Identify the blood parasite species.
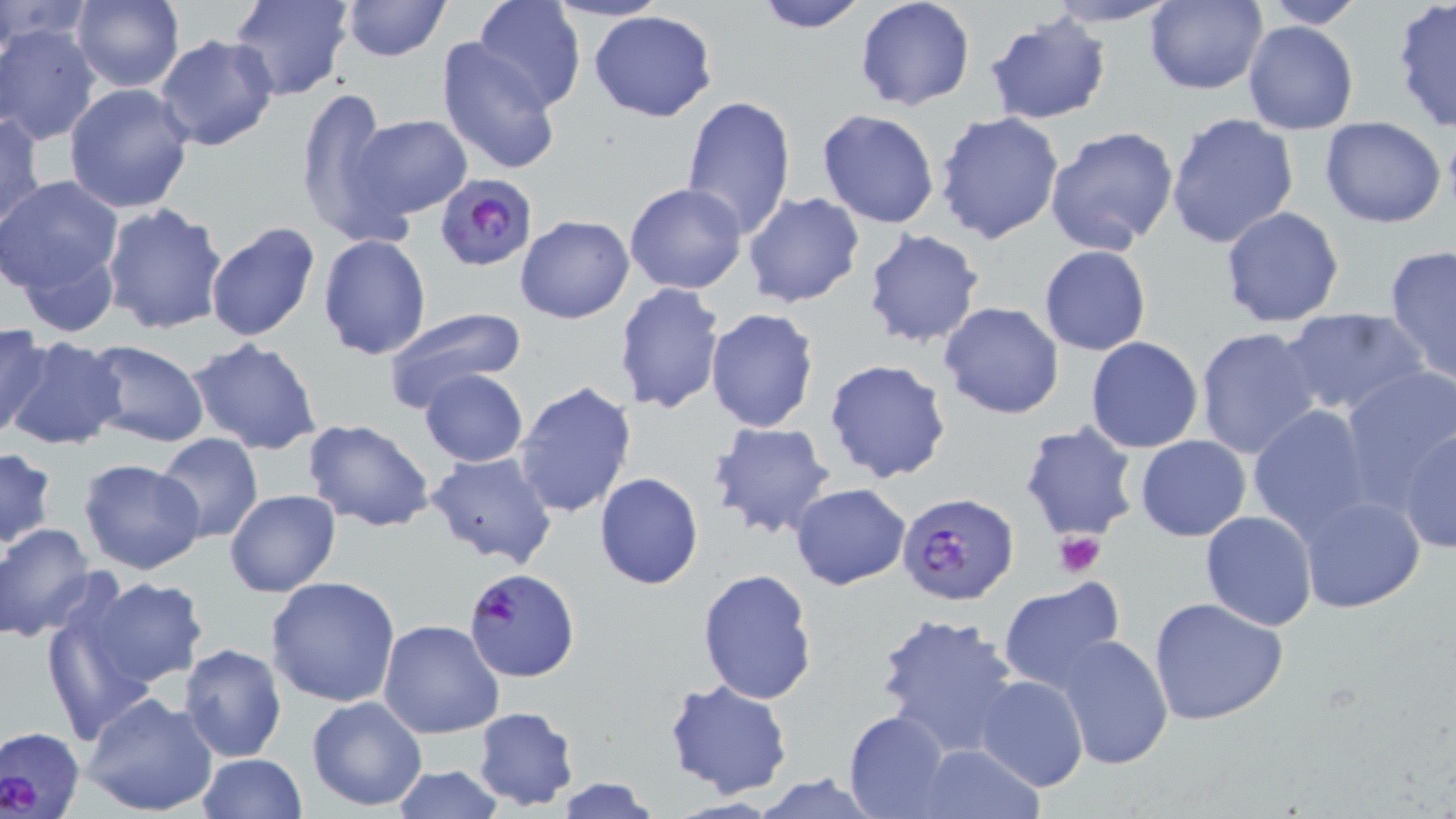

Plasmodium falciparum.

Summary:
  - Coordinate format: approximate bounding boxes as [x1, y1, x2, y2] in pixels
  - Plasmodium falciparum-infected red blood cell locations: [437, 173, 535, 270], [897, 493, 1018, 606], [463, 567, 580, 682], [2, 724, 87, 816]
  - Platelet locations: [1055, 530, 1105, 576]
  - Uninfected red blood cell locations: [1, 0, 90, 55], [71, 0, 184, 91], [229, 0, 352, 101], [339, 0, 450, 61], [473, 0, 585, 110], [546, 0, 668, 24], [751, 0, 870, 34], [855, 0, 976, 113], [1142, 0, 1268, 95], [1258, 0, 1369, 28], [1044, 1, 1184, 27], [1391, 2, 1456, 133], [588, 9, 719, 123], [984, 13, 1112, 126], [1243, 20, 1359, 135], [2, 22, 100, 146], [154, 35, 278, 153], [437, 39, 563, 177], [65, 81, 197, 213], [296, 88, 392, 237], [681, 94, 798, 238], [817, 109, 941, 229], [1, 110, 47, 232], [934, 111, 1064, 247], [1166, 112, 1300, 251], [352, 114, 471, 218], [1319, 116, 1447, 229], [1045, 125, 1180, 255], [2, 175, 124, 293], [624, 183, 747, 295], [743, 193, 866, 309], [100, 203, 230, 336], [1221, 207, 1345, 329], [516, 215, 634, 324], [204, 221, 322, 344], [861, 229, 985, 348], [317, 234, 431, 358], [11, 244, 121, 340], [1383, 244, 1456, 386], [1039, 245, 1151, 355], [613, 281, 726, 416], [939, 302, 1066, 420], [703, 306, 819, 432], [1281, 306, 1431, 420], [381, 307, 528, 418], [0, 322, 52, 439], [1194, 326, 1323, 460], [4, 337, 126, 454], [1085, 337, 1204, 453], [186, 338, 322, 454], [79, 340, 211, 449], [824, 357, 952, 485], [1338, 367, 1456, 508], [419, 369, 528, 468], [515, 381, 637, 520], [1247, 404, 1378, 540], [303, 419, 437, 532], [1018, 420, 1140, 542], [706, 421, 837, 540], [1398, 427, 1455, 554], [154, 432, 264, 543], [1135, 435, 1250, 540], [0, 448, 58, 551], [424, 451, 559, 569], [77, 458, 206, 575], [594, 473, 705, 590], [790, 483, 911, 589], [225, 489, 342, 597], [1297, 494, 1425, 613], [1200, 510, 1318, 631], [0, 524, 96, 641], [695, 568, 818, 704], [77, 576, 209, 690], [266, 576, 400, 706], [997, 580, 1127, 693], [37, 583, 169, 743], [1148, 596, 1289, 725], [875, 610, 1021, 758], [379, 619, 505, 738], [1054, 634, 1174, 771], [179, 644, 287, 762], [99, 657, 288, 786], [974, 674, 1088, 791], [665, 677, 795, 800], [82, 691, 219, 817], [306, 695, 427, 811], [473, 706, 580, 811], [844, 710, 952, 818], [912, 744, 1045, 818], [197, 752, 306, 818], [390, 765, 506, 819], [550, 777, 663, 818]
  - Stain: May-Grünwald-Giemsa
  - Magnification: 1000x
  - Preparation: thin blood film
  - Field of view: single
  - Image size: 1456×819 pixels
  - Modality: light microscopy